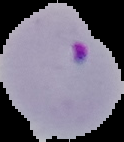
result = Plasmodium parasites detected
image type = segmented cell region on a black background
preparation = thin blood smear
image size = 124×142 pixels